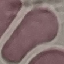

result = no malaria parasites detected
capture = smartphone camera at the microscope eyepiece
stain = Giemsa
preparation = thin blood film
image type = automatically extracted cell patch, resized to 64 × 64 pixels